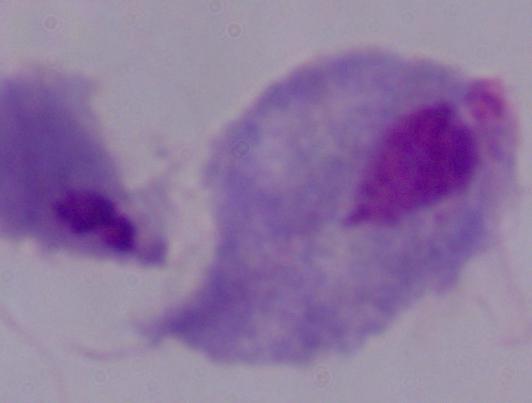

Summary:
  - Modality: photomicrograph
  - Magnification: 1000x
  - Identification: trichomonad